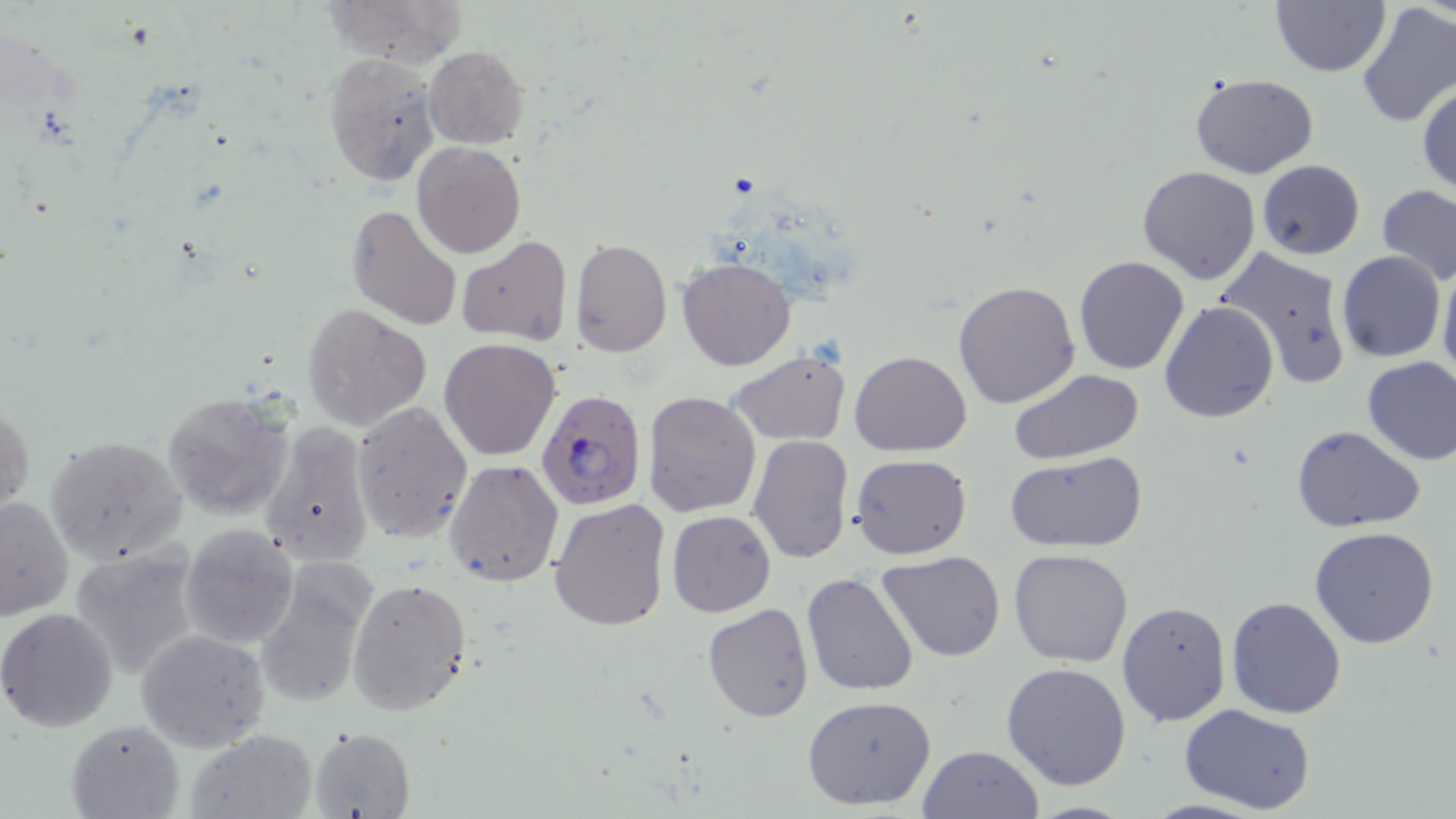
slide-level diagnosis = Plasmodium falciparum
modality = light microscopy
Plasmodium falciparum-infected red blood cell locations = approximate bounding boxes as (x1,y1)-(x2,y2) corner pairs in pixels: (535,390)-(648,511)
field of view = one of a larger specimen
image size = 1456×819 pixels
preparation = thin blood smear
stain = May-Grünwald-Giemsa
magnification = 1000x
uninfected red blood cell locations = approximate bounding boxes as (x1,y1)-(x2,y2) corner pairs in pixels: (325,0)-(462,67), (1271,0)-(1392,76), (1353,4)-(1456,128), (425,46)-(529,147), (323,52)-(439,186), (1190,72)-(1320,179), (1417,82)-(1456,197), (413,142)-(524,258), (1256,159)-(1365,259), (1136,165)-(1262,284), (1376,184)-(1456,288), (347,204)-(463,332), (457,236)-(572,346), (572,238)-(672,357), (1214,244)-(1354,391), (1338,250)-(1445,362), (1074,255)-(1189,375), (677,257)-(797,371), (1438,259)-(1456,388), (952,279)-(1081,409), (1159,300)-(1280,423), (302,303)-(432,431), (439,338)-(561,461), (725,350)-(851,445), (849,351)-(972,457), (1361,357)-(1456,466), (1008,368)-(1144,463), (160,391)-(296,520), (643,391)-(760,516), (1,396)-(33,526), (350,401)-(472,543), (260,420)-(374,567), (1290,425)-(1426,531), (44,433)-(190,563), (747,435)-(856,563), (1005,449)-(1148,551), (850,454)-(971,560), (444,460)-(565,588), (0,496)-(73,621), (548,498)-(671,632), (667,510)-(776,616), (180,522)-(300,650), (1310,525)-(1439,648), (67,545)-(202,680), (1008,547)-(1134,666), (876,552)-(1006,661), (254,564)-(374,711), (800,571)-(921,697), (347,576)-(472,716), (1227,596)-(1346,719), (1117,601)-(1231,726), (702,602)-(814,723), (1,607)-(120,732), (138,629)-(270,751), (1002,662)-(1132,790), (801,694)-(937,811), (1179,703)-(1319,817), (65,718)-(182,818), (308,727)-(416,819), (183,731)-(316,817), (916,745)-(1043,819)